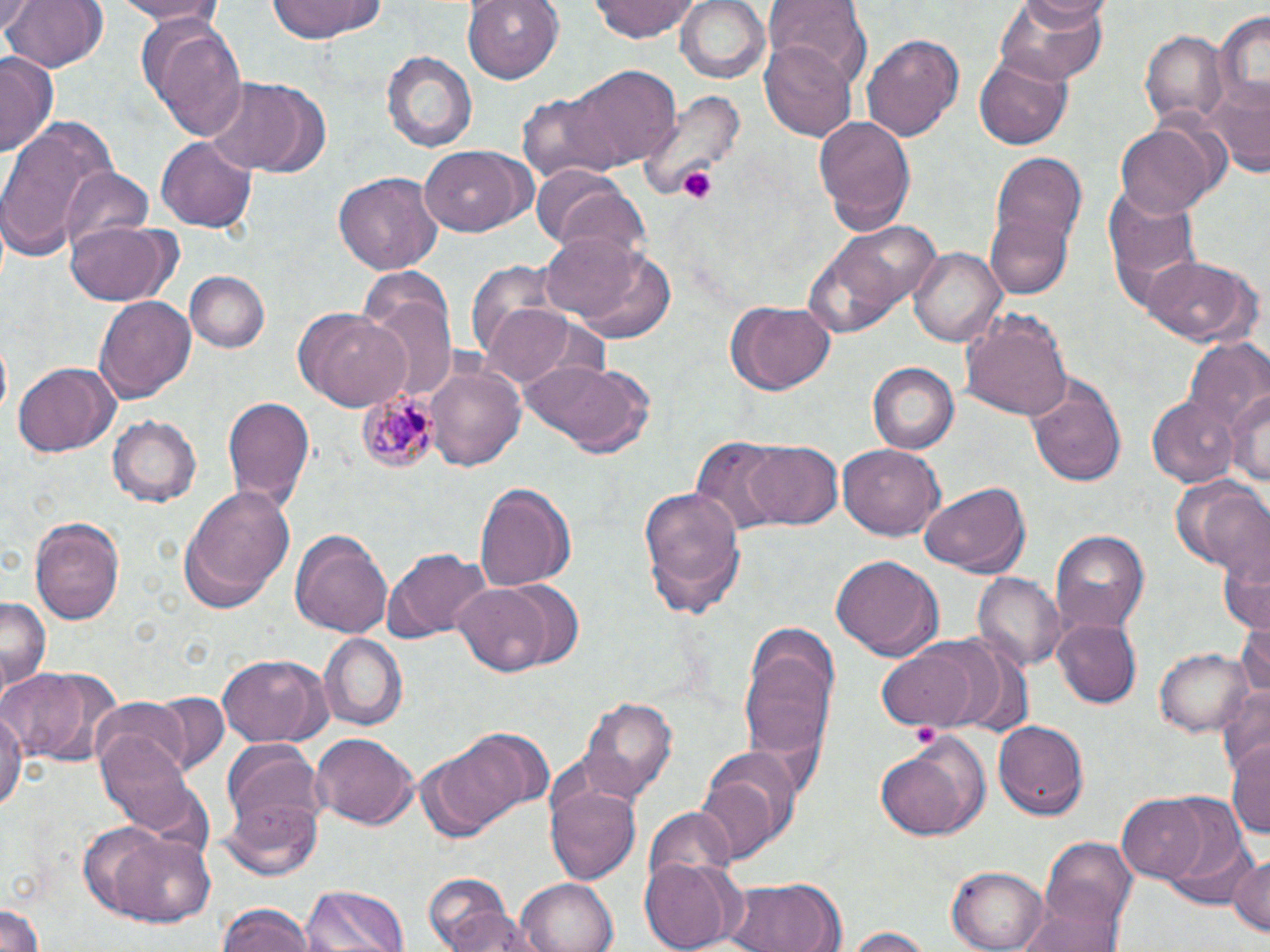

Summary:
  - Coordinate format: approximate bounding boxes as (x1, y1, x2, y2) in pixels
  - Plasmodium malariae-infected red blood cell locations: (358, 391, 440, 475)
  - Platelet locations: (675, 163, 718, 204), (910, 720, 942, 751)
  - Uninfected red blood cell locations: (2, 0, 106, 73), (104, 0, 230, 26), (264, 0, 385, 43), (463, 0, 563, 83), (589, 0, 702, 43), (677, 0, 770, 84), (996, 0, 1109, 90), (1018, 0, 1104, 33), (764, 2, 869, 87), (0, 5, 29, 42), (1213, 10, 1270, 114), (139, 17, 248, 140), (1138, 22, 1228, 131), (861, 32, 966, 143), (761, 38, 858, 142), (382, 51, 478, 156), (0, 54, 57, 154), (974, 56, 1076, 152), (559, 67, 680, 173), (206, 77, 328, 177), (637, 87, 741, 202), (1215, 88, 1268, 179), (813, 113, 918, 235), (0, 118, 113, 260), (1117, 124, 1217, 219), (155, 136, 256, 233), (420, 144, 535, 236), (990, 150, 1089, 275), (58, 168, 155, 261), (332, 171, 443, 277), (538, 176, 652, 263), (1102, 182, 1203, 309), (987, 211, 1072, 301), (799, 218, 937, 337), (65, 224, 175, 307), (566, 241, 681, 348), (909, 246, 1005, 350), (1140, 254, 1255, 346), (464, 260, 569, 368), (185, 271, 270, 352), (357, 280, 457, 409), (96, 295, 197, 405), (476, 300, 589, 388), (726, 301, 836, 397), (960, 305, 1074, 421), (296, 308, 414, 413), (1182, 336, 1270, 437), (516, 358, 658, 459), (13, 360, 119, 457), (423, 361, 527, 472), (868, 362, 958, 454), (1025, 372, 1128, 488), (1227, 383, 1270, 490), (1144, 395, 1238, 486), (222, 398, 314, 514), (108, 415, 201, 506), (691, 437, 792, 537), (737, 438, 844, 531), (838, 443, 945, 542), (1168, 476, 1265, 571), (474, 481, 578, 592), (918, 482, 1032, 579), (177, 483, 295, 613), (636, 484, 746, 616), (29, 518, 125, 624), (290, 528, 393, 642), (1051, 530, 1150, 636), (1217, 536, 1269, 634), (381, 548, 489, 642), (830, 554, 944, 662), (974, 573, 1064, 669), (496, 578, 585, 669), (453, 584, 553, 676), (0, 595, 49, 693), (1237, 616, 1270, 704), (1054, 618, 1141, 707), (320, 635, 407, 729), (740, 639, 838, 777), (874, 643, 985, 733), (1154, 645, 1254, 737), (216, 653, 333, 746), (0, 664, 118, 769), (1218, 685, 1270, 776), (115, 693, 225, 777), (577, 694, 679, 803), (0, 703, 25, 816), (994, 721, 1091, 819), (423, 728, 552, 838), (96, 732, 203, 840), (311, 733, 418, 829), (873, 737, 987, 842), (1228, 742, 1270, 841), (220, 745, 328, 866), (693, 753, 796, 866), (545, 777, 642, 888), (1118, 795, 1211, 883), (1153, 795, 1252, 896), (643, 806, 740, 887), (98, 828, 218, 927), (1040, 837, 1137, 934), (1227, 855, 1270, 939), (639, 857, 742, 949), (951, 865, 1050, 952), (423, 872, 519, 952), (723, 875, 844, 952), (514, 877, 619, 952), (300, 882, 410, 952), (1015, 893, 1124, 952), (0, 900, 45, 951), (215, 903, 317, 952), (840, 927, 935, 952)
  - Slide-level diagnosis: Plasmodium malariae
  - Image size: 1270×952 pixels
  - Stain: May-Grünwald-Giemsa
  - Field of view: single
  - Magnification: 1000x
  - Preparation: thin blood smear
  - Modality: optical microscopy